Assess the morphology of the erythrocytes.
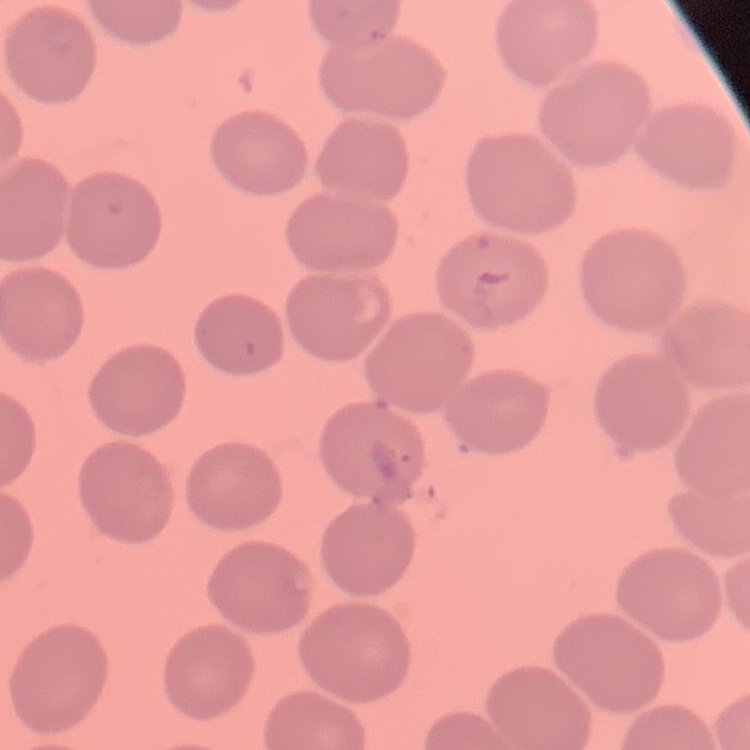

They show no rouleaux formation.

Summary:
  - Image type: square crop of a larger photomicrograph
  - Stain: Field's or Giemsa
  - Preparation: thin peripheral smear